Comment on the morphology of the erythrocytes.
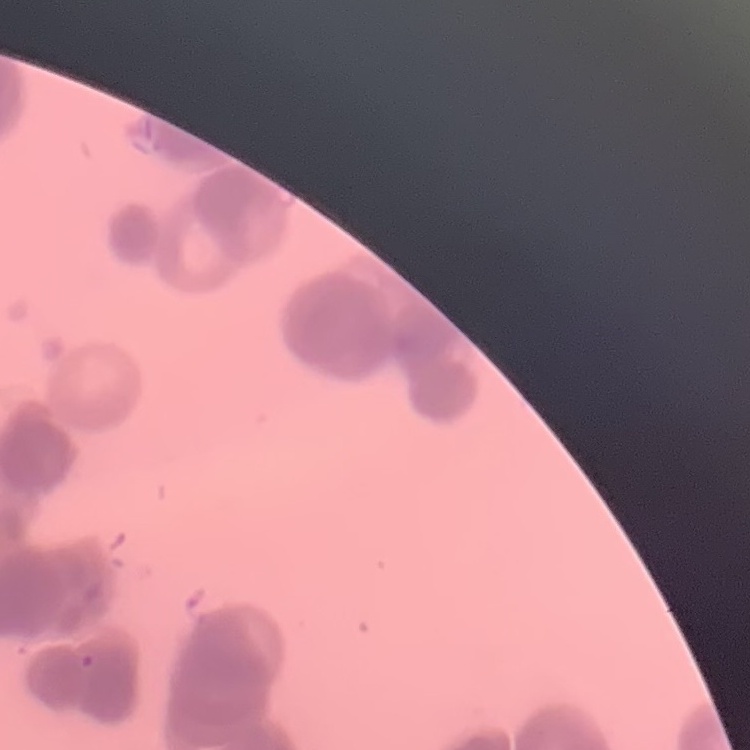

Rouleaux formation.

Summary:
  - Stain: Field's or Giemsa
  - Image type: one tile cut from a larger photomicrograph
  - Preparation: thin blood film